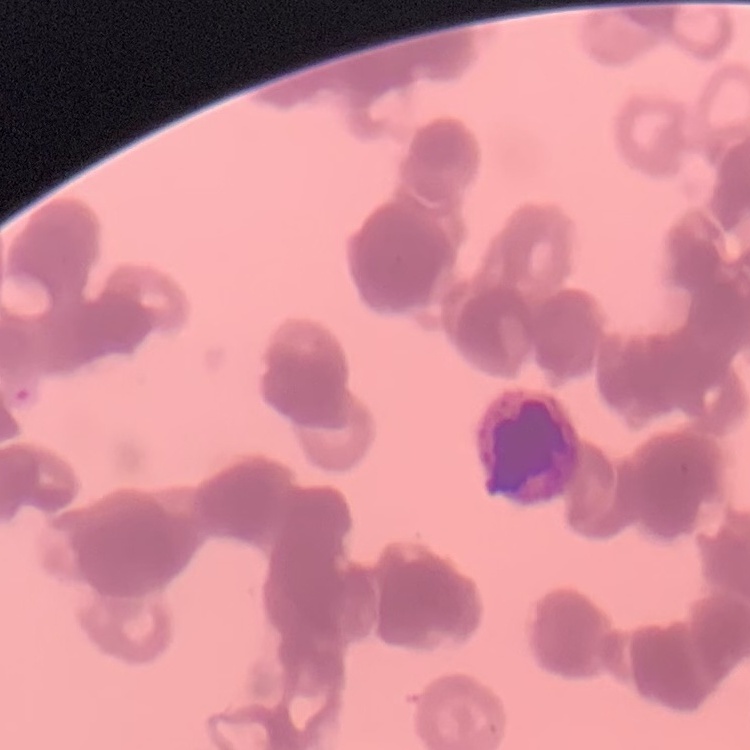

The red blood cells exhibit rouleaux formation. Stained with either Field's or Giemsa. Thin blood smear. Square crop of a larger photomicrograph.